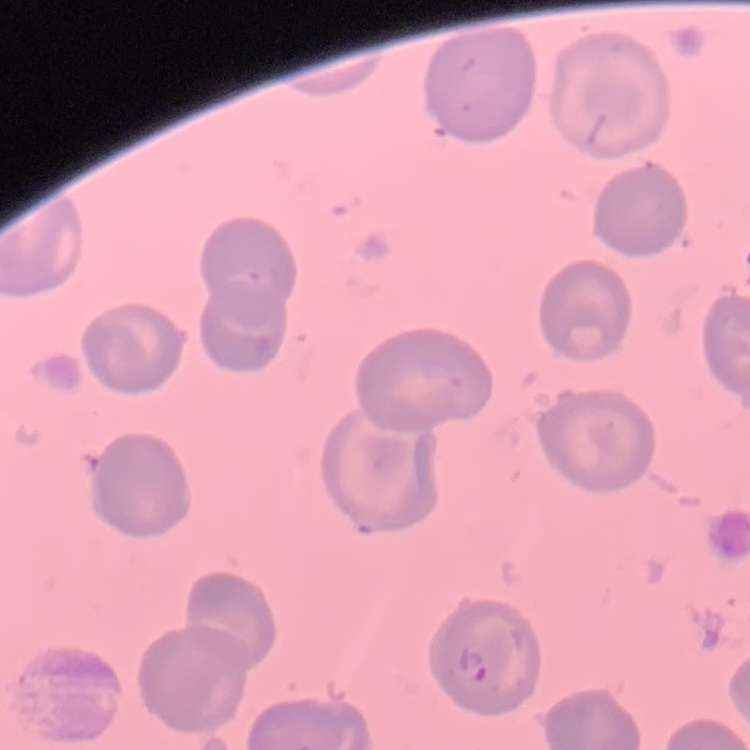
red blood cell morphology = no rouleaux formation
stain = Field's or Giemsa
image type = square crop of a larger photomicrograph
preparation = thin peripheral smear